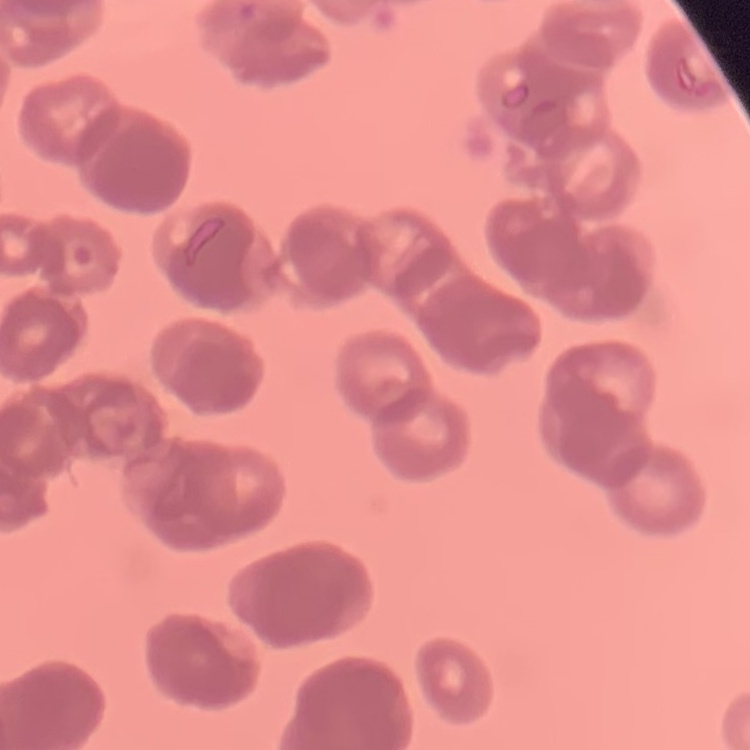

erythrocyte morphology = rouleaux formation
preparation = thin peripheral smear
image type = one tile cut from a larger photomicrograph
stain = Field's or Giemsa